Describe the morphology of the red blood cells.
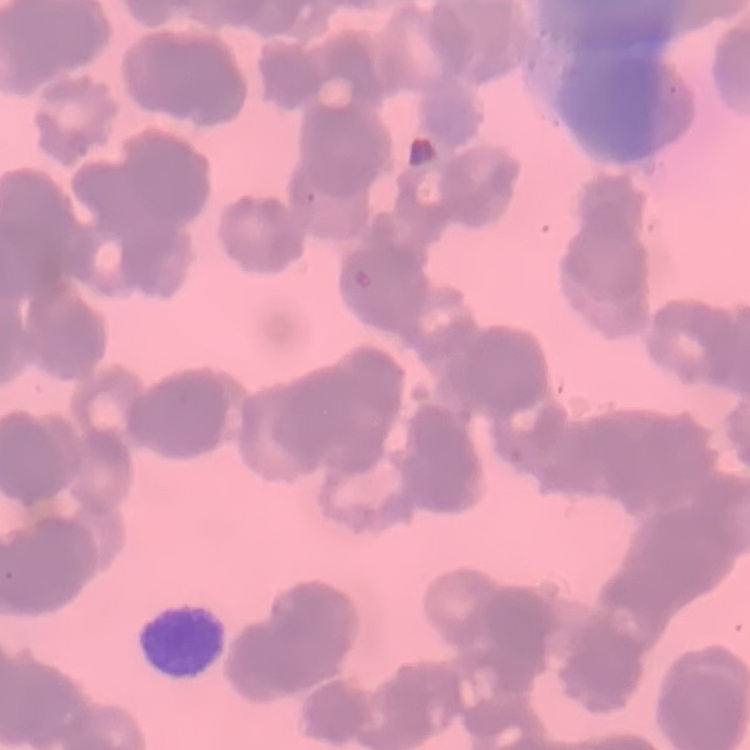
They show rouleaux formation.

One tile cut from a larger photomicrograph. Thin peripheral smear. Stained with either Field's or Giemsa.